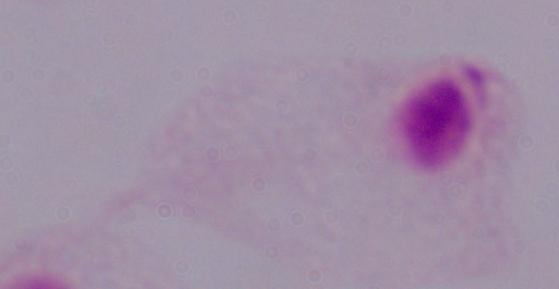

A trichomonad is shown. Captured at 1000x magnification. Photomicrograph.